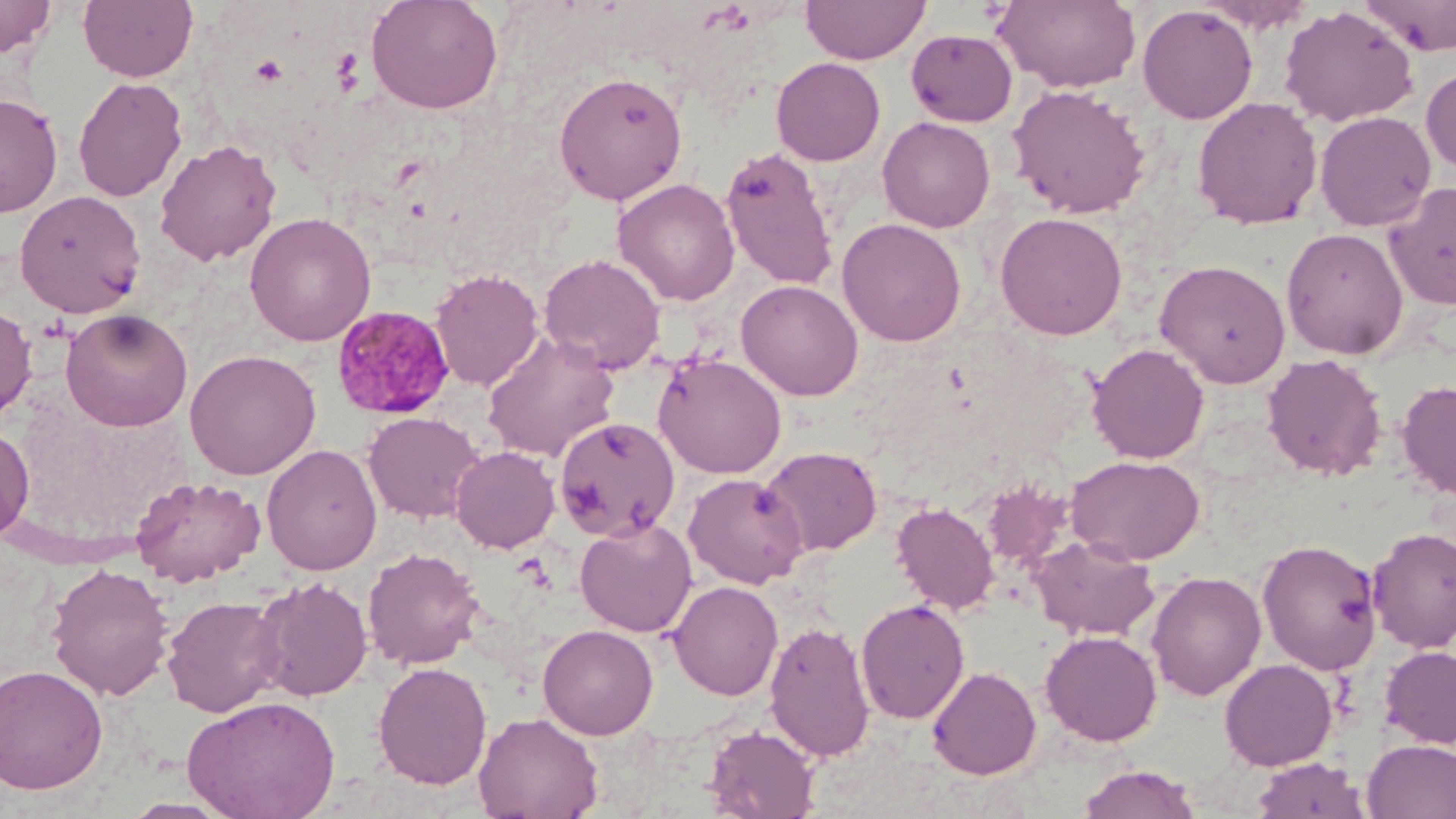

Summary:
  - Coordinate format: approximate bounding boxes as (x1,y1)-(x2,y2) corner pairs in pixels
  - Platelet locations: (252,55)-(287,85)
  - Uninfected red blood cell locations: (0,0)-(56,58), (78,0)-(197,82), (366,0)-(503,115), (800,0)-(931,65), (994,0)-(1141,93), (1357,0)-(1456,56), (1196,1)-(1316,32), (1137,5)-(1258,124), (1280,6)-(1419,127), (906,28)-(1018,126), (771,57)-(886,165), (1421,65)-(1456,175), (553,71)-(689,206), (73,76)-(187,202), (1007,84)-(1151,219), (0,93)-(63,217), (1191,96)-(1323,230), (1315,111)-(1436,231), (877,116)-(995,232), (155,139)-(282,266), (720,146)-(840,290), (612,178)-(740,306), (1384,182)-(1456,310), (14,190)-(146,318), (994,211)-(1127,340), (244,212)-(377,346), (837,218)-(966,347), (1281,228)-(1409,359), (538,253)-(667,374), (1154,259)-(1291,389), (430,268)-(544,391), (736,279)-(863,400), (0,302)-(37,423), (60,307)-(193,432), (482,331)-(620,462), (1087,343)-(1209,464), (184,349)-(322,479), (653,352)-(787,479), (1261,353)-(1387,481), (1397,380)-(1456,501), (363,411)-(484,523), (554,417)-(679,541), (0,424)-(35,543), (261,443)-(383,575), (451,446)-(560,553), (760,446)-(882,558), (1066,455)-(1205,564), (683,472)-(809,589), (130,475)-(265,586), (980,481)-(1074,569), (892,502)-(999,615), (574,518)-(697,637), (1366,526)-(1456,653), (1028,534)-(1160,640), (1257,539)-(1382,675), (362,547)-(485,670), (46,562)-(175,700), (1146,571)-(1266,701), (251,576)-(373,702), (668,580)-(783,700), (163,595)-(286,717), (856,599)-(970,724), (763,619)-(875,762), (538,624)-(658,740), (1040,630)-(1162,745), (1379,646)-(1456,748), (1219,658)-(1337,770), (372,661)-(493,789), (1,663)-(108,795), (927,666)-(1042,780), (182,694)-(341,819), (474,711)-(603,819), (703,725)-(820,818), (1362,740)-(1456,819), (1250,757)-(1370,819), (1076,764)-(1201,819)
  - Plasmodium malariae-infected red blood cell locations: (331,305)-(454,419)
  - Slide-level diagnosis: Plasmodium malariae
  - Magnification: 1000x
  - Preparation: thin blood smear
  - Field of view: one of a larger specimen
  - Modality: optical microscopy
  - Stain: May-Grünwald-Giemsa
  - Image size: 1456×819 pixels